Locate every Plasmodium falciparum-infected red blood cell.
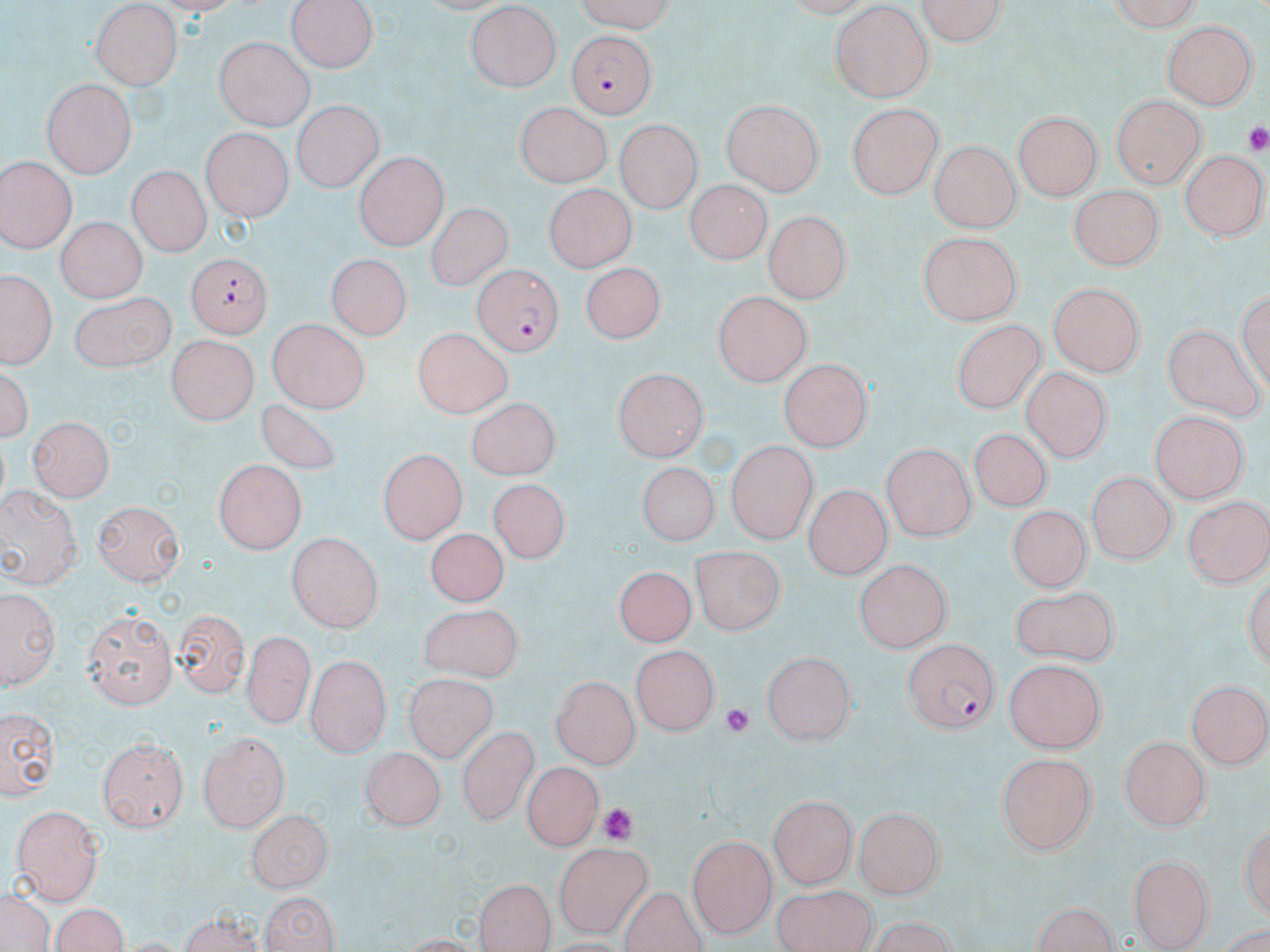

Approximate bounding boxes as named x1/y1/x2/y2 corners in pixels.
Plasmodium falciparum-infected red blood cells: (x1=569, y1=32, x2=655, y2=120), (x1=187, y1=252, x2=270, y2=338), (x1=472, y1=263, x2=563, y2=356), (x1=904, y1=639, x2=1000, y2=734).

Summary:
  - Platelet locations: (x1=1244, y1=119, x2=1270, y2=151), (x1=722, y1=702, x2=757, y2=742), (x1=598, y1=803, x2=638, y2=843)
  - Uninfected red blood cell locations: (x1=571, y1=0, x2=675, y2=29), (x1=911, y1=0, x2=1010, y2=47), (x1=1100, y1=0, x2=1201, y2=30), (x1=289, y1=2, x2=377, y2=73), (x1=92, y1=4, x2=183, y2=91), (x1=464, y1=5, x2=563, y2=94), (x1=828, y1=6, x2=933, y2=101), (x1=226, y1=9, x2=369, y2=101), (x1=1163, y1=20, x2=1256, y2=112), (x1=213, y1=36, x2=312, y2=130), (x1=40, y1=79, x2=138, y2=174), (x1=1113, y1=96, x2=1202, y2=190), (x1=721, y1=100, x2=823, y2=196), (x1=290, y1=103, x2=385, y2=191), (x1=514, y1=104, x2=615, y2=185), (x1=846, y1=104, x2=942, y2=201), (x1=1013, y1=110, x2=1100, y2=202), (x1=614, y1=122, x2=700, y2=214), (x1=199, y1=129, x2=293, y2=219), (x1=929, y1=137, x2=1020, y2=230), (x1=1180, y1=146, x2=1264, y2=240), (x1=356, y1=152, x2=447, y2=249), (x1=0, y1=157, x2=76, y2=253), (x1=125, y1=166, x2=209, y2=257), (x1=687, y1=179, x2=768, y2=262), (x1=544, y1=183, x2=636, y2=272), (x1=1068, y1=187, x2=1160, y2=271), (x1=424, y1=203, x2=510, y2=291), (x1=764, y1=210, x2=852, y2=304), (x1=54, y1=217, x2=144, y2=302), (x1=916, y1=232, x2=1026, y2=327), (x1=328, y1=257, x2=408, y2=341), (x1=176, y1=261, x2=266, y2=401), (x1=579, y1=266, x2=668, y2=345), (x1=1, y1=274, x2=52, y2=365), (x1=1047, y1=280, x2=1147, y2=374), (x1=73, y1=291, x2=174, y2=373), (x1=710, y1=292, x2=810, y2=386), (x1=264, y1=320, x2=367, y2=411), (x1=950, y1=320, x2=1049, y2=413), (x1=1161, y1=323, x2=1263, y2=421), (x1=409, y1=328, x2=516, y2=421), (x1=165, y1=336, x2=261, y2=420), (x1=3, y1=358, x2=34, y2=450), (x1=777, y1=358, x2=874, y2=452), (x1=613, y1=367, x2=710, y2=461), (x1=1020, y1=369, x2=1111, y2=460), (x1=261, y1=399, x2=341, y2=471), (x1=467, y1=399, x2=557, y2=480), (x1=1149, y1=410, x2=1246, y2=503), (x1=25, y1=417, x2=115, y2=500), (x1=971, y1=426, x2=1055, y2=510), (x1=724, y1=442, x2=817, y2=542), (x1=879, y1=444, x2=978, y2=539), (x1=377, y1=449, x2=466, y2=543), (x1=215, y1=460, x2=306, y2=554), (x1=639, y1=460, x2=717, y2=543), (x1=1087, y1=471, x2=1172, y2=565), (x1=487, y1=480, x2=569, y2=567), (x1=803, y1=483, x2=890, y2=579), (x1=0, y1=488, x2=83, y2=589), (x1=1183, y1=493, x2=1270, y2=588), (x1=96, y1=500, x2=184, y2=585), (x1=1006, y1=506, x2=1088, y2=592), (x1=422, y1=526, x2=507, y2=610), (x1=286, y1=534, x2=381, y2=634), (x1=691, y1=545, x2=783, y2=634), (x1=856, y1=559, x2=954, y2=651), (x1=616, y1=564, x2=696, y2=645), (x1=1013, y1=584, x2=1120, y2=664), (x1=3, y1=592, x2=55, y2=688), (x1=418, y1=605, x2=520, y2=683), (x1=82, y1=609, x2=177, y2=705), (x1=176, y1=609, x2=246, y2=698), (x1=244, y1=630, x2=308, y2=729), (x1=633, y1=643, x2=718, y2=733), (x1=763, y1=650, x2=859, y2=744), (x1=305, y1=653, x2=391, y2=754), (x1=1005, y1=661, x2=1103, y2=752), (x1=551, y1=673, x2=641, y2=769), (x1=403, y1=677, x2=504, y2=764), (x1=1187, y1=677, x2=1270, y2=769), (x1=2, y1=708, x2=55, y2=795), (x1=457, y1=722, x2=538, y2=829), (x1=197, y1=731, x2=288, y2=831), (x1=1120, y1=735, x2=1212, y2=829), (x1=99, y1=736, x2=187, y2=830), (x1=359, y1=745, x2=441, y2=827), (x1=996, y1=753, x2=1099, y2=857), (x1=522, y1=760, x2=600, y2=848), (x1=770, y1=794, x2=857, y2=889), (x1=11, y1=802, x2=104, y2=905), (x1=856, y1=807, x2=942, y2=898), (x1=246, y1=811, x2=330, y2=894), (x1=687, y1=832, x2=779, y2=938), (x1=551, y1=843, x2=653, y2=933), (x1=1129, y1=854, x2=1213, y2=952), (x1=474, y1=876, x2=555, y2=952), (x1=0, y1=886, x2=55, y2=952), (x1=769, y1=886, x2=884, y2=952), (x1=260, y1=889, x2=338, y2=952), (x1=1031, y1=900, x2=1124, y2=952), (x1=48, y1=903, x2=129, y2=952), (x1=173, y1=911, x2=267, y2=950), (x1=859, y1=921, x2=965, y2=951)
  - Slide-level diagnosis: Plasmodium falciparum
  - Magnification: 1000x
  - Image size: 1270×952 pixels
  - Field of view: one of a larger specimen
  - Stain: May-Grünwald-Giemsa
  - Preparation: thin blood film
  - Modality: light microscopy